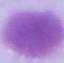

Summary:
  - Identification: red blood cell
  - Modality: micrograph
  - Magnification: 1000x